Assess this cell for malaria.
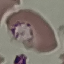

It is parasitized.

preparation = thin blood smear
stain = Giemsa
image type = automatically extracted cell patch, resized to 64 × 64 pixels
capture = smartphone through the microscope eyepiece